Outline each blood parasite and name the species.
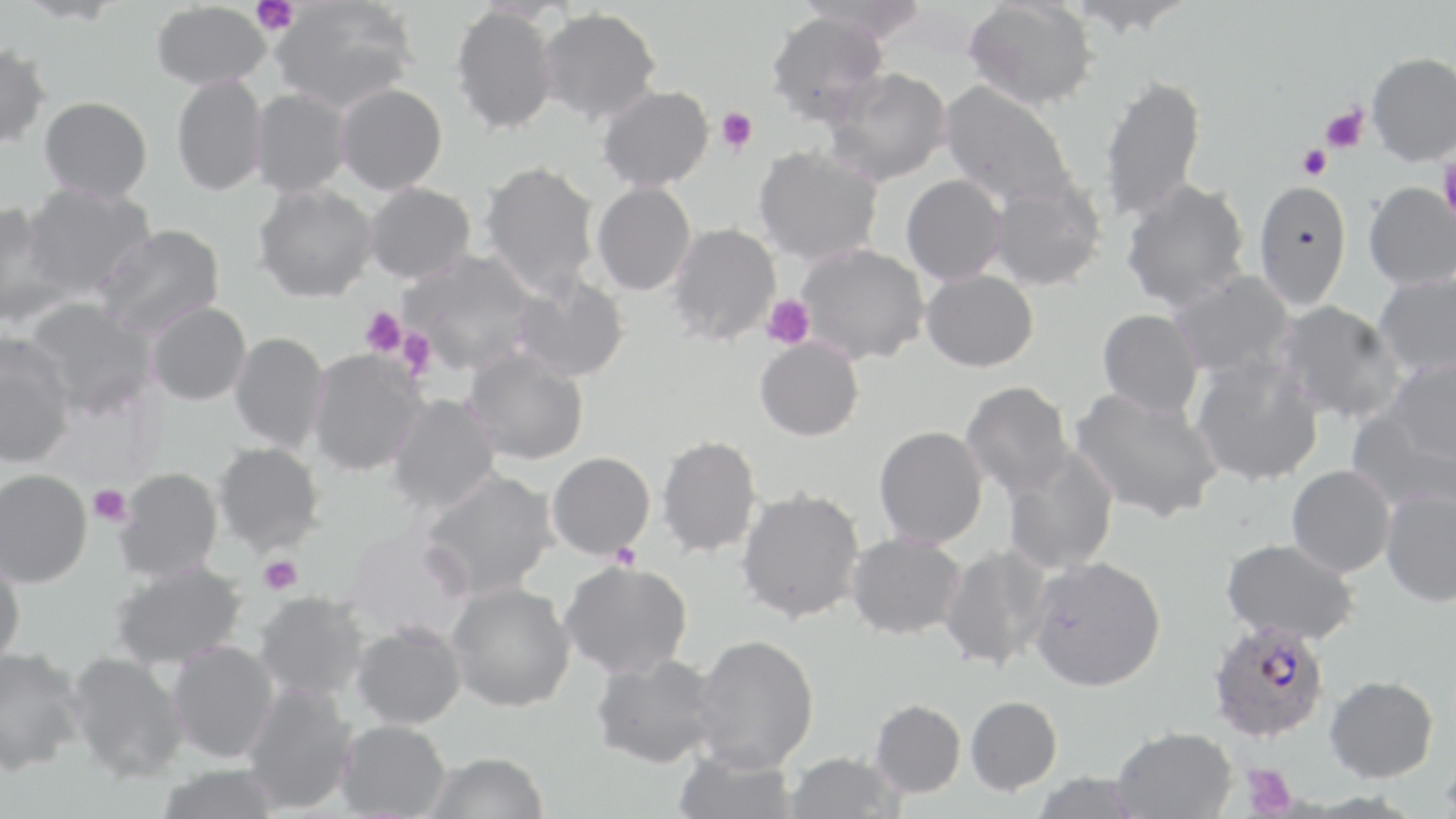
Approximate bounding boxes as (x1, y1, x2, y2) in pixels.
Plasmodium falciparum-infected red blood cells: (1207, 619, 1330, 743).
No Plasmodium ovale, Plasmodium malariae, Plasmodium vivax, Babesia divergens, or Trypanosoma brucei observed.

Uninfected red blood cell locations: (269, 0, 418, 113), (798, 0, 932, 42), (964, 0, 1098, 111), (1065, 0, 1197, 37), (151, 2, 272, 90), (450, 4, 561, 135), (537, 7, 662, 125), (766, 11, 889, 127), (0, 43, 52, 152), (1367, 51, 1456, 166), (824, 67, 952, 187), (1097, 73, 1207, 223), (171, 74, 269, 196), (938, 81, 1076, 209), (335, 82, 448, 195), (597, 85, 714, 192), (248, 88, 352, 198), (39, 96, 152, 203), (753, 145, 883, 266), (480, 160, 601, 298), (901, 174, 1008, 285), (987, 176, 1107, 292), (1120, 178, 1251, 312), (1252, 178, 1352, 311), (592, 181, 696, 296), (1363, 181, 1456, 290), (253, 182, 379, 303), (364, 182, 476, 284), (22, 183, 157, 300), (0, 206, 77, 328), (666, 222, 781, 347), (93, 224, 226, 338), (795, 243, 929, 365), (398, 250, 538, 374), (921, 268, 1039, 372), (1168, 271, 1297, 380), (1372, 272, 1456, 377), (509, 274, 629, 384), (21, 296, 159, 420), (1272, 299, 1404, 424), (145, 301, 251, 405), (1097, 308, 1204, 418), (229, 331, 330, 453), (754, 337, 864, 441), (0, 338, 76, 469), (464, 347, 589, 465), (305, 349, 428, 477), (1190, 355, 1324, 487), (1387, 356, 1456, 464), (960, 380, 1074, 499), (1069, 387, 1225, 524), (386, 393, 500, 515), (1346, 410, 1456, 516), (874, 425, 989, 549), (657, 434, 763, 559), (213, 441, 325, 554), (1001, 446, 1120, 575), (547, 451, 656, 559), (1286, 465, 1396, 578), (114, 467, 224, 584), (0, 468, 92, 588), (419, 469, 559, 600), (736, 487, 865, 626), (1379, 489, 1456, 607), (340, 526, 474, 643), (846, 533, 967, 639), (1221, 537, 1360, 644), (939, 545, 1052, 672), (0, 552, 26, 668), (1027, 555, 1167, 691), (559, 560, 693, 680), (110, 561, 247, 670), (446, 581, 576, 712), (254, 592, 371, 701), (351, 622, 467, 729), (693, 633, 819, 772), (167, 640, 279, 763), (0, 646, 86, 775), (66, 650, 189, 783), (590, 652, 720, 769), (1324, 674, 1439, 782), (240, 682, 359, 815), (965, 695, 1062, 794), (870, 699, 966, 798), (336, 719, 452, 819), (1112, 726, 1237, 819), (672, 749, 799, 819), (1439, 749, 1456, 815), (423, 752, 549, 819), (783, 752, 906, 818), (155, 763, 282, 819), (1029, 771, 1144, 819). Platelet locations: (252, 0, 299, 36), (1319, 105, 1369, 153), (716, 106, 758, 154), (1296, 143, 1332, 181), (1438, 158, 1456, 225), (762, 295, 815, 350), (360, 306, 407, 357), (397, 328, 436, 379), (88, 485, 133, 527), (609, 542, 642, 570), (258, 556, 302, 595), (1242, 763, 1297, 817). Slide-level diagnosis: Plasmodium falciparum. Optical microscopy. 1000x magnification. May-Grünwald-Giemsa-stained preparation. Image is 1456×819 pixels. Thin blood film. One field of a larger specimen.